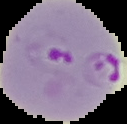

From a thin blood smear. The area outside the segmented cell region is set to black. Image is 127×124 pixels. Result: malaria parasites detected.